Name the parasite shown.
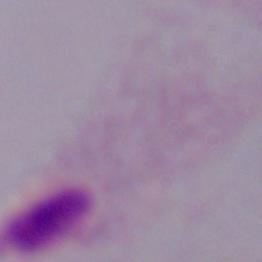

A trichomonad.

Micrograph. Captured at 1000x magnification.